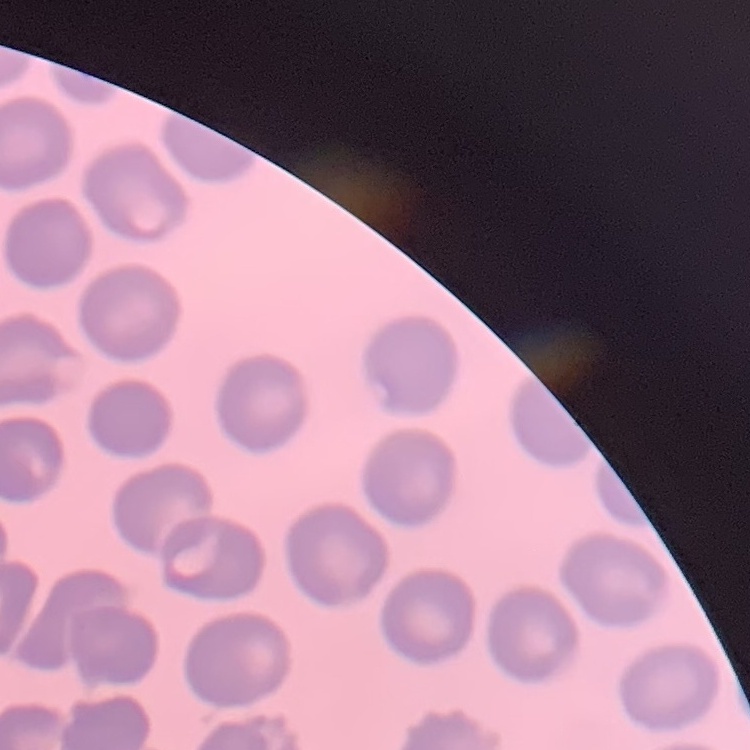
{
  "erythrocyte_morphology": "no rouleaux formation",
  "preparation": "thin peripheral smear",
  "image_type": "one tile cut from a larger photomicrograph",
  "stain": "Field's or Giemsa"
}